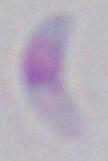

modality: photomicrograph
identification: Toxoplasma gondii
magnification: 1000x